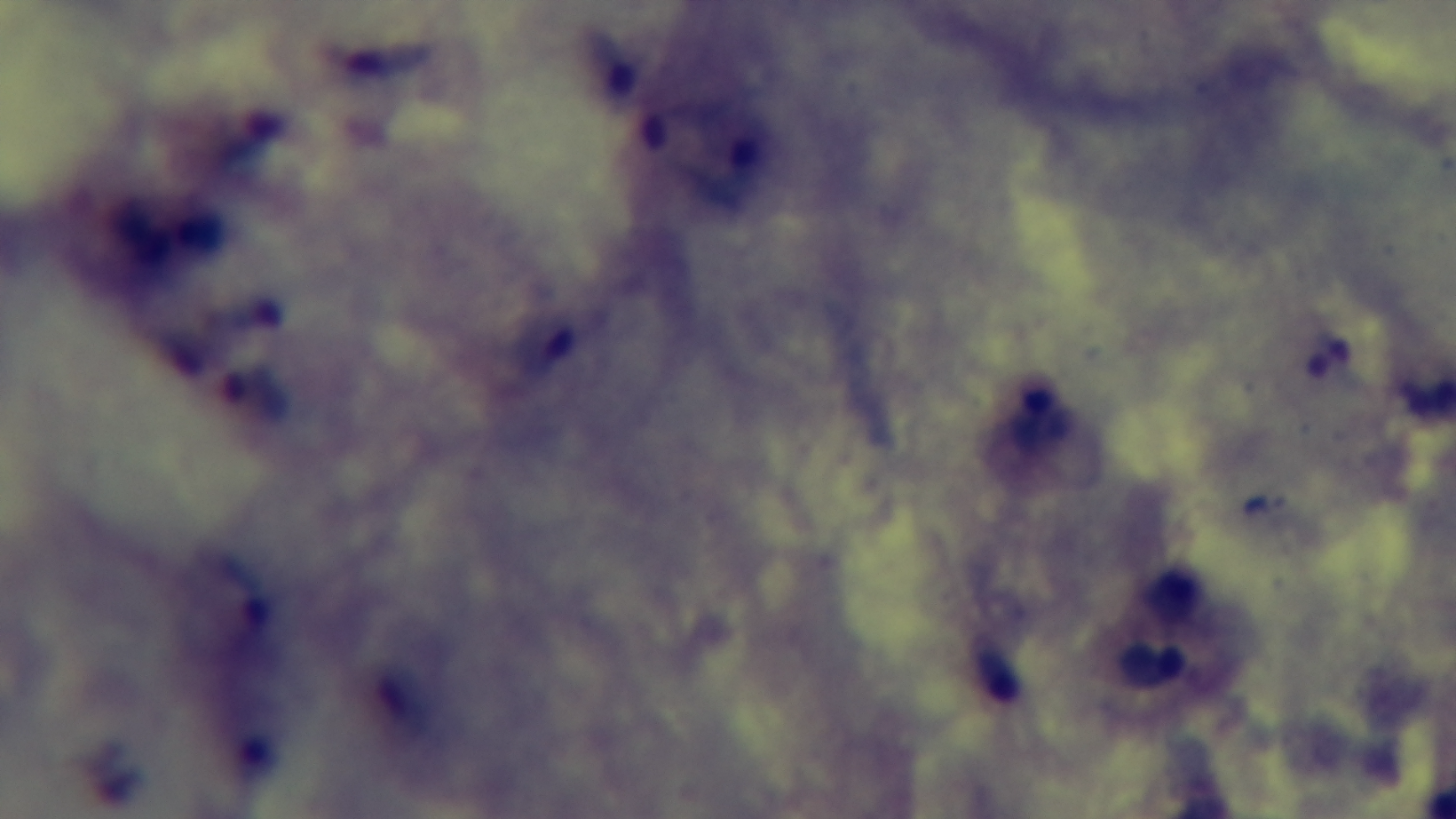
Summary:
  - Malaria status: positive
  - Stain: Giemsa
  - Field of view: single
  - Objective: 100x oil immersion
  - Capture: mounted 4K digital camera
  - Modality: light microscopy
  - Preparation: thick blood film